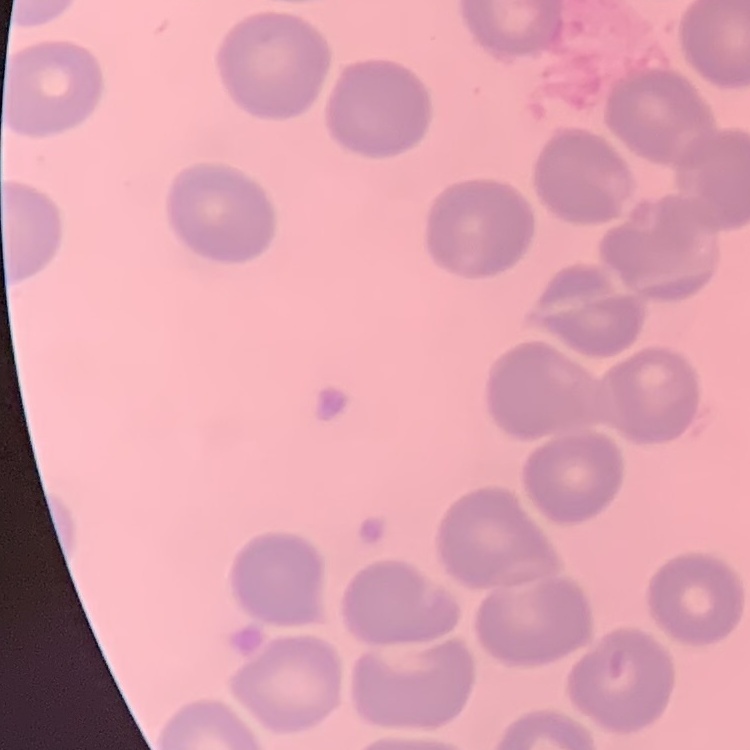

red blood cell morphology = no rouleaux formation
stain = Field's or Giemsa
preparation = thin blood smear
image type = square crop of a larger photomicrograph